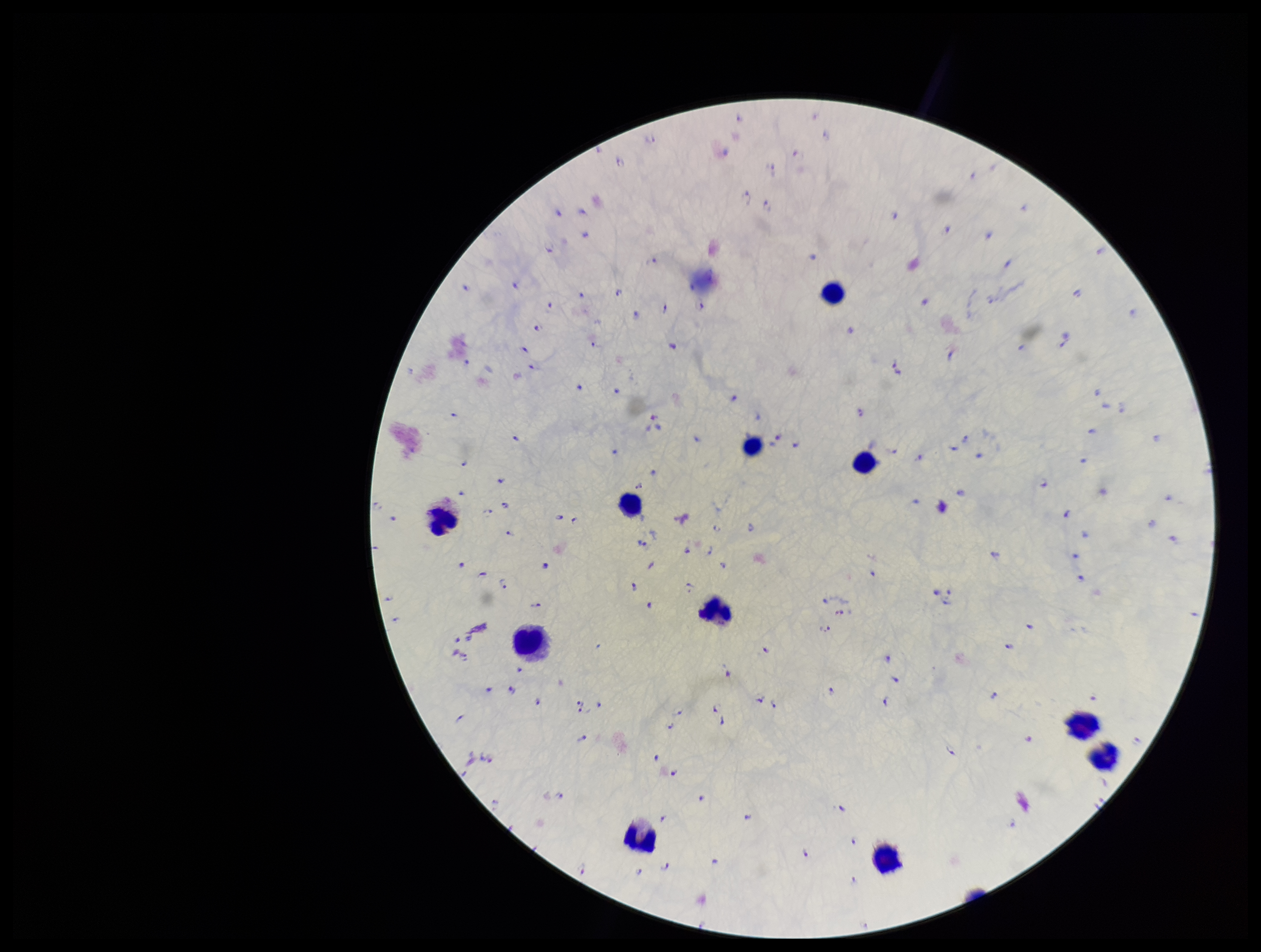

Summary:
  - Species reported for this patient: Plasmodium falciparum
  - Parasite count: 172
  - Capture: smartphone photograph through the microscope eyepiece
  - Image size: 1261×952 pixels
  - Plasmodium parasites: detected
  - Stain: Giemsa
  - Field of view: one from this slide
  - Preparation: thick blood smear
  - Leukocyte count: 11
  - Patient malaria status: positive